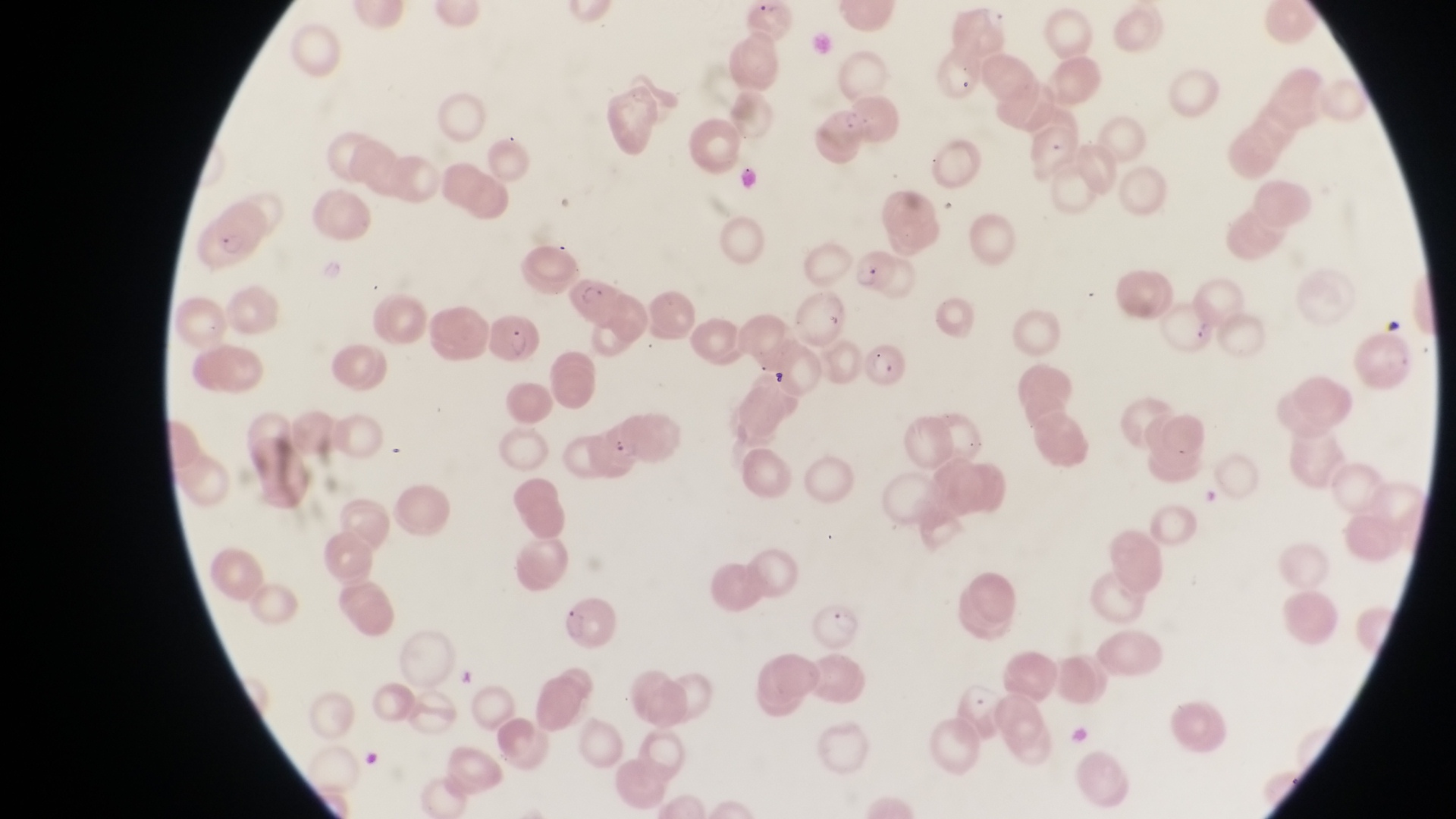

preparation = thin blood film
parasitised red blood cell locations = approximate bounding boxes as {left, top, right, bottom} in pixels: {812, 102, 870, 166}, {211, 202, 275, 263}, {846, 244, 894, 292}, {566, 275, 621, 322}, {491, 311, 540, 361}, {867, 338, 912, 390}, {561, 599, 615, 651}, {809, 602, 864, 649}
magnification = 1000x
image size = 1456×819 pixels
country = Uganda
capture = smartphone photograph through the eyepiece of an Olympus CX-23 microscope
field of view = single